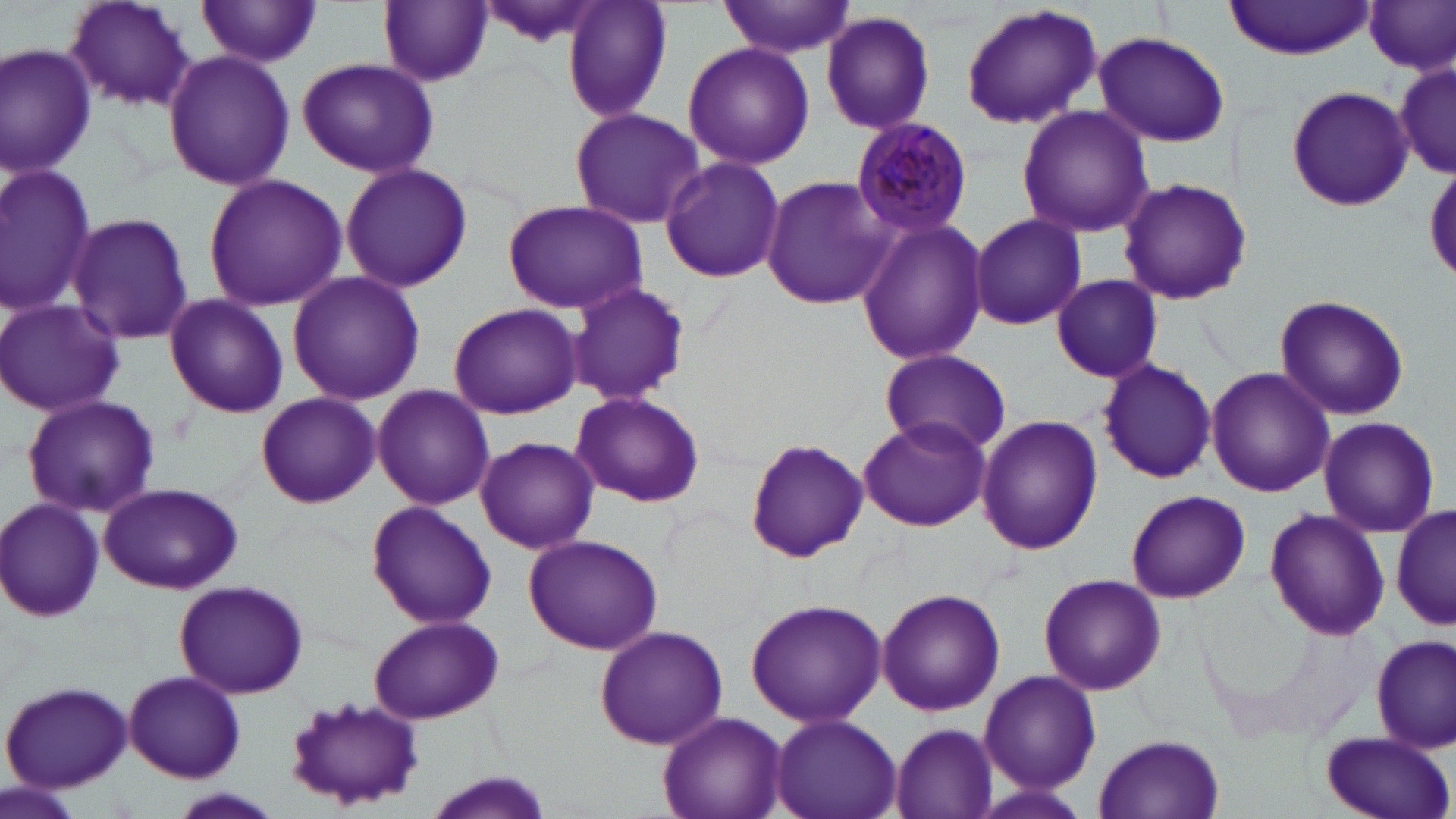
Approximate bounding boxes as named x1/y1/x2/y2 corners in pixels. Plasmodium malariae-infected red blood cell locations: (x1=851, y1=117, x2=974, y2=239). Uninfected red blood cell locations: (x1=62, y1=0, x2=197, y2=110), (x1=375, y1=0, x2=494, y2=88), (x1=471, y1=0, x2=602, y2=48), (x1=562, y1=0, x2=675, y2=121), (x1=719, y1=0, x2=854, y2=59), (x1=197, y1=1, x2=326, y2=71), (x1=1225, y1=1, x2=1375, y2=59), (x1=1363, y1=2, x2=1456, y2=76), (x1=958, y1=3, x2=1103, y2=131), (x1=821, y1=9, x2=936, y2=135), (x1=1093, y1=31, x2=1231, y2=148), (x1=682, y1=42, x2=815, y2=171), (x1=0, y1=43, x2=95, y2=181), (x1=162, y1=50, x2=295, y2=190), (x1=296, y1=58, x2=439, y2=179), (x1=1394, y1=65, x2=1456, y2=175), (x1=1285, y1=85, x2=1414, y2=213), (x1=1016, y1=104, x2=1153, y2=237), (x1=569, y1=107, x2=706, y2=230), (x1=657, y1=157, x2=785, y2=284), (x1=339, y1=163, x2=473, y2=292), (x1=0, y1=165, x2=99, y2=314), (x1=760, y1=172, x2=896, y2=311), (x1=203, y1=173, x2=346, y2=311), (x1=1118, y1=176, x2=1252, y2=306), (x1=500, y1=198, x2=647, y2=314), (x1=65, y1=210, x2=195, y2=347), (x1=967, y1=212, x2=1087, y2=331), (x1=853, y1=218, x2=990, y2=367), (x1=287, y1=271, x2=424, y2=405), (x1=1050, y1=273, x2=1164, y2=383), (x1=563, y1=280, x2=692, y2=408), (x1=163, y1=294, x2=289, y2=419), (x1=1273, y1=294, x2=1410, y2=421), (x1=0, y1=299, x2=124, y2=418), (x1=448, y1=302, x2=583, y2=420), (x1=876, y1=348, x2=1013, y2=457), (x1=1095, y1=357, x2=1217, y2=485), (x1=1205, y1=366, x2=1333, y2=498), (x1=370, y1=385, x2=497, y2=511), (x1=257, y1=392, x2=379, y2=508), (x1=570, y1=393, x2=703, y2=505), (x1=21, y1=394, x2=161, y2=520), (x1=858, y1=415, x2=991, y2=533), (x1=976, y1=415, x2=1102, y2=556), (x1=1315, y1=417, x2=1440, y2=538), (x1=475, y1=435, x2=599, y2=554), (x1=743, y1=436, x2=869, y2=563), (x1=97, y1=484, x2=244, y2=595), (x1=1125, y1=489, x2=1250, y2=605), (x1=0, y1=498, x2=105, y2=623), (x1=1390, y1=498, x2=1455, y2=638), (x1=366, y1=499, x2=497, y2=629), (x1=1263, y1=507, x2=1391, y2=642), (x1=523, y1=533, x2=664, y2=654), (x1=1037, y1=572, x2=1167, y2=696), (x1=173, y1=580, x2=309, y2=699), (x1=876, y1=588, x2=1005, y2=718), (x1=743, y1=598, x2=886, y2=726), (x1=367, y1=613, x2=507, y2=725), (x1=1250, y1=623, x2=1395, y2=745), (x1=594, y1=626, x2=729, y2=751), (x1=1370, y1=634, x2=1454, y2=753), (x1=978, y1=668, x2=1101, y2=794), (x1=124, y1=670, x2=246, y2=783), (x1=2, y1=680, x2=134, y2=792), (x1=283, y1=694, x2=424, y2=809), (x1=658, y1=712, x2=786, y2=819), (x1=769, y1=713, x2=901, y2=819), (x1=890, y1=722, x2=999, y2=818), (x1=1319, y1=730, x2=1453, y2=819), (x1=1094, y1=733, x2=1226, y2=818), (x1=420, y1=773, x2=557, y2=819), (x1=2, y1=779, x2=88, y2=819), (x1=164, y1=788, x2=285, y2=819). Slide-level diagnosis: Plasmodium malariae. Light microscopy. Image is 1456×819 pixels. 1000x magnification. May-Grünwald-Giemsa stain. Thin blood film. Single field of view.